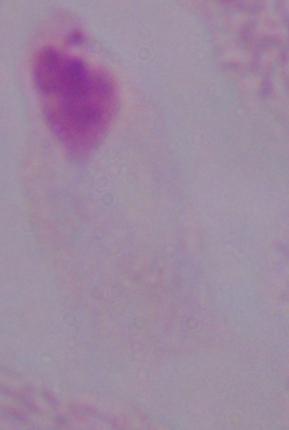

Summary:
  - Identification: trichomonad
  - Modality: micrograph
  - Magnification: 1000x